Look for Plasmodium parasites.
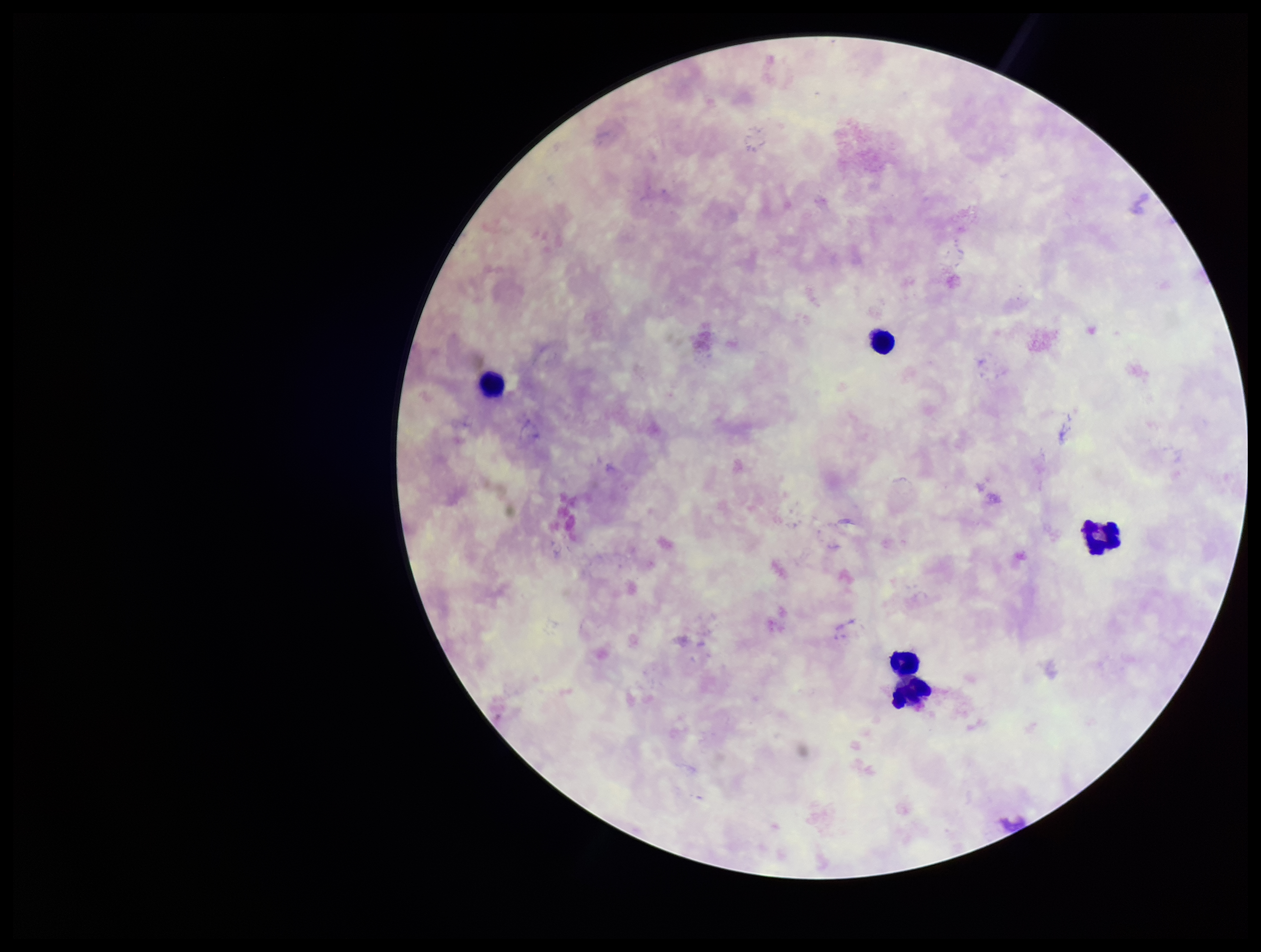
None seen.

{
  "parasite_count": 0,
  "field_of_view": "one from this slide",
  "preparation": "thick smear",
  "image_size": "1261×952 pixels",
  "capture": "smartphone photograph through the microscope eyepiece",
  "stain": "Giemsa",
  "leukocyte_count": 5,
  "patient_malaria_status": "negative"
}